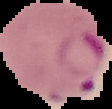
Summary:
  - Image size: 112×109 pixels
  - Malaria status: parasitized
  - Image type: cell region segmented out of the field of view; surrounding area masked to black
  - Preparation: thin blood film